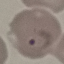
Summary:
  - Malaria status: parasitized
  - Preparation: thin smear
  - Image type: cell patch, automatically extracted from a larger field of view and resized to 64 × 64 pixels
  - Stain: Giemsa
  - Capture: smartphone through the microscope eyepiece